Identify the blood parasite species.
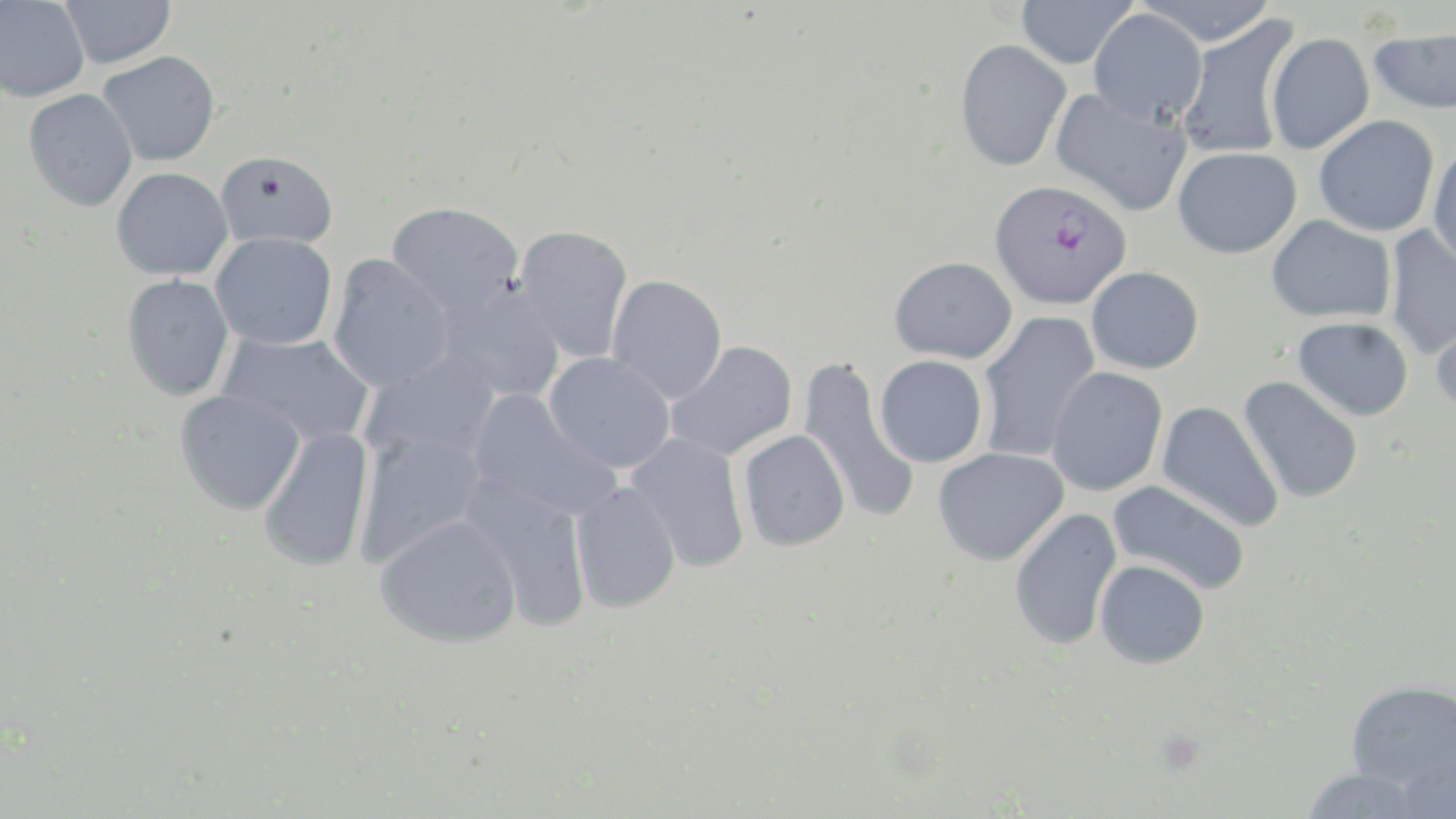
Plasmodium falciparum.

Summary:
  - Coordinate format: approximate bounding boxes as [x1, y1, x2, y2] in pixels
  - Plasmodium falciparum-infected red blood cell locations: [990, 179, 1130, 309]
  - Uninfected red blood cell locations: [59, 0, 176, 69], [1016, 0, 1136, 69], [1133, 0, 1279, 46], [0, 1, 90, 102], [1088, 9, 1207, 126], [1176, 14, 1301, 160], [1368, 27, 1456, 114], [1265, 32, 1374, 154], [955, 39, 1071, 171], [98, 51, 220, 166], [1049, 88, 1192, 216], [23, 89, 138, 212], [1313, 115, 1439, 237], [1427, 144, 1456, 268], [1173, 147, 1301, 258], [215, 150, 338, 249], [111, 167, 233, 281], [387, 202, 524, 319], [1267, 215, 1396, 323], [1384, 223, 1456, 360], [513, 225, 634, 364], [210, 232, 337, 350], [326, 254, 454, 392], [889, 256, 1017, 364], [1086, 266, 1204, 374], [121, 274, 235, 402], [606, 275, 728, 403], [433, 281, 566, 404], [1431, 304, 1456, 417], [976, 311, 1100, 463], [1293, 317, 1413, 421], [217, 332, 375, 447], [664, 341, 798, 462], [358, 352, 501, 471], [544, 352, 676, 473], [874, 355, 988, 468], [796, 357, 921, 526], [1046, 368, 1168, 496], [1238, 377, 1364, 504], [175, 389, 305, 514], [465, 390, 621, 525], [1156, 401, 1285, 533], [257, 425, 375, 573], [353, 429, 488, 569], [738, 430, 851, 552], [625, 432, 750, 573], [933, 447, 1068, 565], [458, 474, 593, 632], [1107, 480, 1250, 597], [569, 481, 682, 614], [1009, 507, 1122, 651], [375, 514, 522, 648], [1094, 559, 1210, 669], [1345, 680, 1456, 792], [1396, 749, 1456, 817], [1299, 767, 1430, 818]
  - Preparation: thin blood smear
  - Modality: optical microscopy
  - Field of view: single
  - Image size: 1456×819 pixels
  - Stain: May-Grünwald-Giemsa
  - Magnification: 1000x